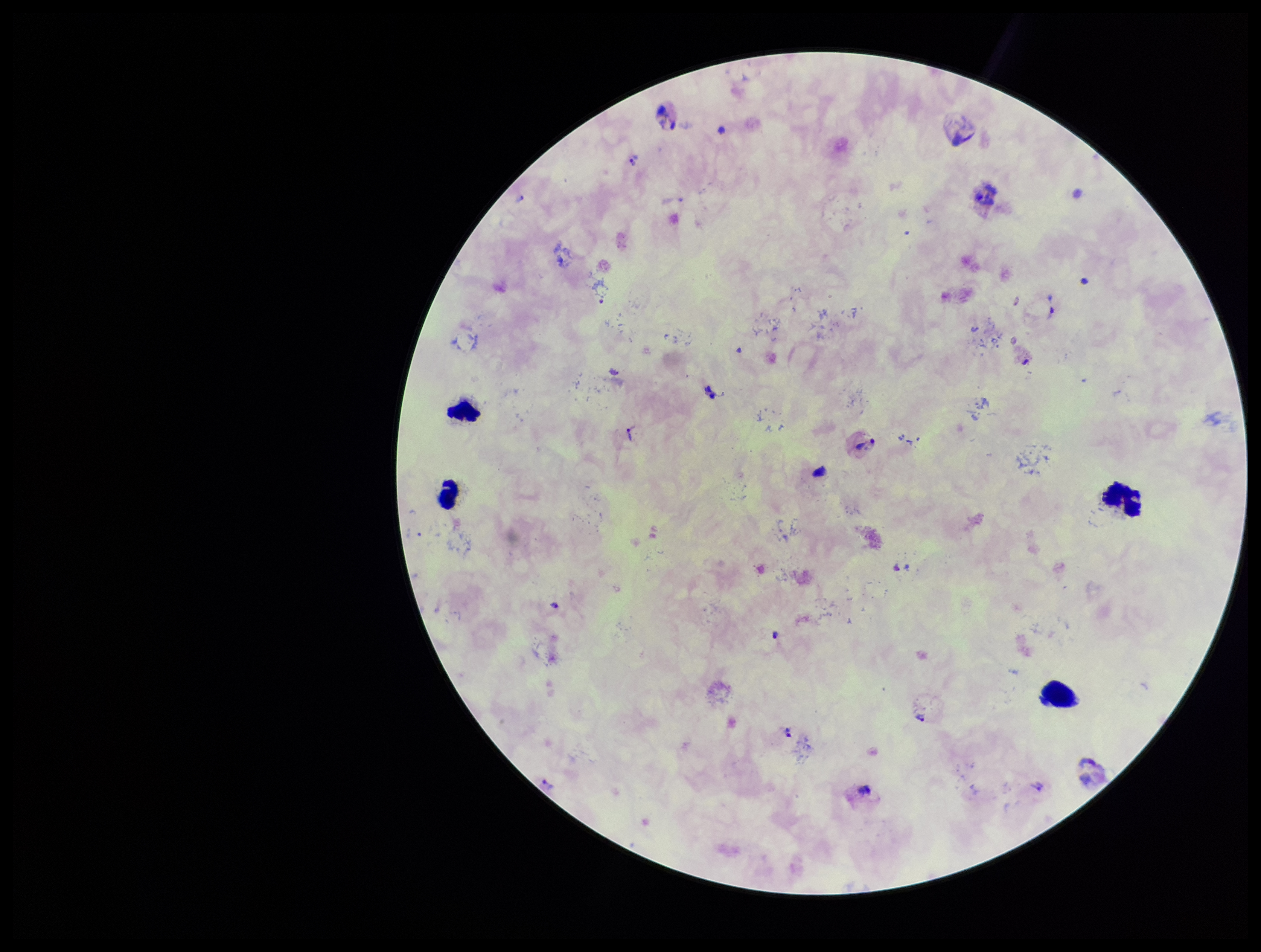

Patient malaria status: infected. Parasite count: 15. Plasmodium parasites: identified. Species reported for this patient: Plasmodium vivax. Single field of view. Preparation: thick smear. Photographed through the microscope eyepiece with a smartphone camera. Image is 1261×952 pixels. Leukocyte count: 4. Stained with Giemsa.